Locate Plasmodium parasites and leukocytes.
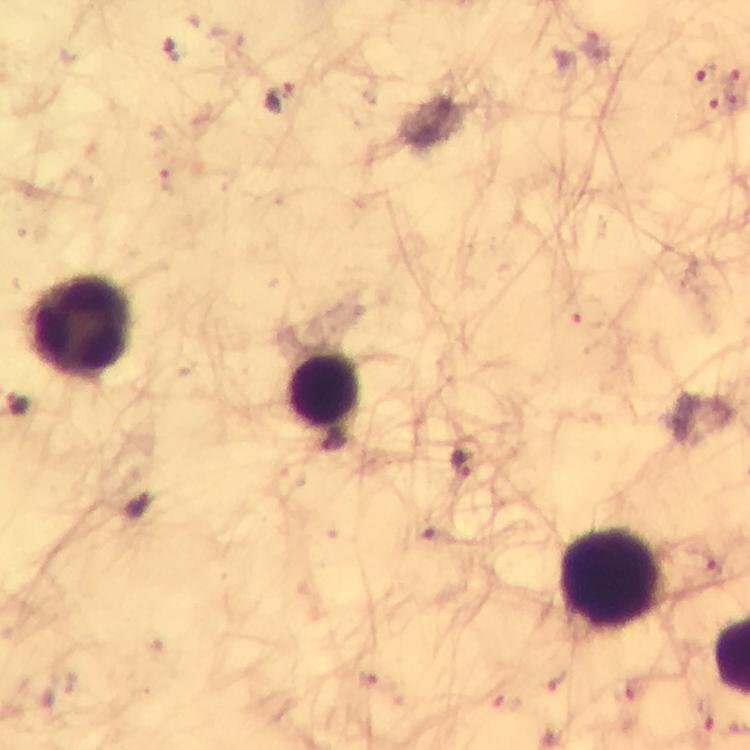

Approximate object centers, in pixels from the top-left corner.
Plasmodium parasites: (x=172, y=50), (x=706, y=71), (x=731, y=73), (x=279, y=98), (x=707, y=110), (x=168, y=183), (x=587, y=313), (x=462, y=464), (x=138, y=507), (x=711, y=567), (x=370, y=680), (x=556, y=680), (x=633, y=695), (x=509, y=704), (x=705, y=717).
Leukocytes: (x=78, y=325), (x=324, y=390), (x=611, y=576).

preparation = thick blood smear
image size = 750×750 pixels
cropped from = one field of view
stain = Giemsa
magnification = 100x
context = from a malaria diagnostic workup
immersion oil = used
capture = smartphone photograph through a microscope